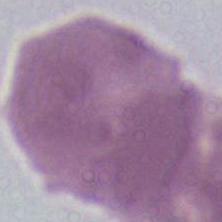
Photomicrograph. A red blood cell is seen. Captured at 1000x magnification.